Classify this cell by malaria status.
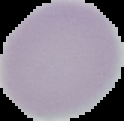
It is uninfected.

{
  "preparation": "thin blood film",
  "image_type": "segmented cell region on a black background",
  "image_size": "124×121 pixels"
}